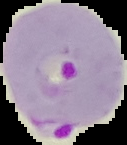
From a thin blood film. Segmented cell region on a black background. Malaria status: parasitized. Image is 127×145 pixels.